Mark where platelets are.
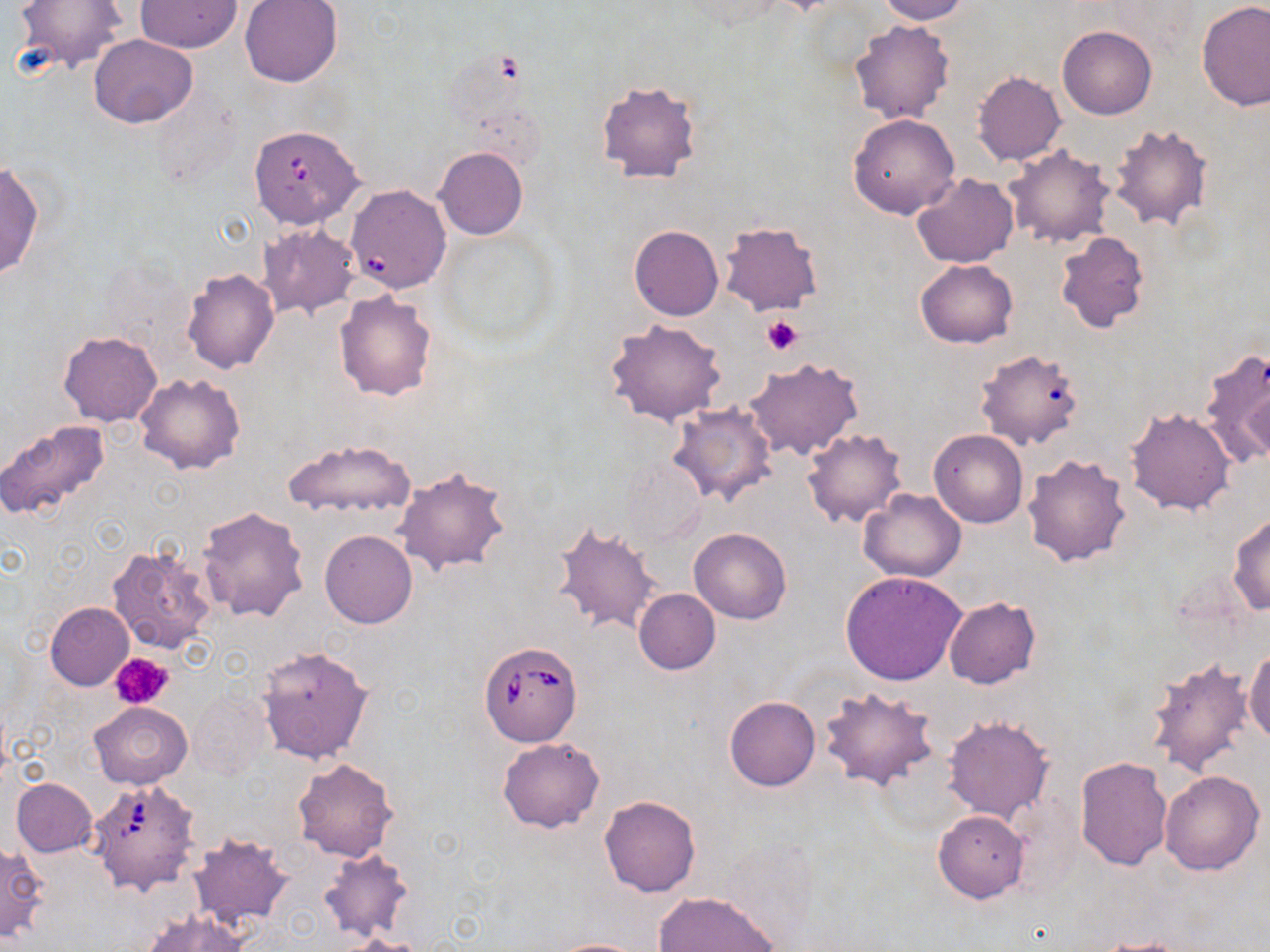

Approximate bounding boxes as (x1,y1)-(x2,y2) corner pairs in pixels.
Platelets: (762,315)-(802,355), (111,652)-(175,710).

Summary:
  - Uninfected red blood cell locations: (14,0)-(128,74), (240,0)-(343,87), (877,0)-(969,24), (136,1)-(241,52), (672,1)-(789,32), (1196,1)-(1270,113), (849,19)-(954,125), (1058,25)-(1156,120), (90,34)-(198,128), (973,71)-(1065,165), (595,79)-(703,185), (849,113)-(959,219), (1107,122)-(1213,231), (1003,145)-(1115,249), (435,147)-(527,241), (0,162)-(43,282), (911,173)-(1019,268), (717,221)-(824,316), (258,222)-(361,319), (629,225)-(723,321), (1054,231)-(1150,333), (915,259)-(1018,348), (181,268)-(280,374), (334,290)-(438,401), (604,319)-(729,428), (58,332)-(162,426), (1200,344)-(1270,468), (974,348)-(1084,450), (742,357)-(863,460), (135,373)-(246,475), (668,404)-(777,505), (1125,406)-(1237,516), (0,421)-(111,524), (802,429)-(908,528), (930,430)-(1029,528), (285,439)-(416,519), (1020,453)-(1132,568), (620,459)-(707,550), (393,466)-(510,575), (859,488)-(966,581), (196,505)-(309,624), (1228,513)-(1270,616), (552,521)-(663,638), (689,528)-(791,624), (320,530)-(417,628), (106,544)-(216,653), (841,570)-(967,686), (634,589)-(720,674), (943,595)-(1041,690), (45,602)-(134,690), (255,646)-(373,764), (1245,647)-(1270,748), (1145,655)-(1256,780), (819,686)-(938,790), (189,688)-(273,780), (724,695)-(820,791), (89,702)-(191,789), (942,714)-(1053,824), (498,737)-(604,833), (1074,757)-(1171,871), (292,758)-(398,862), (1160,769)-(1264,875), (10,778)-(97,857), (598,795)-(701,897), (933,809)-(1030,903), (187,833)-(293,927), (0,843)-(47,941), (320,847)-(414,941), (652,891)-(781,952), (142,911)-(250,952), (345,934)-(428,952), (1084,935)-(1195,951), (544,937)-(651,951)
  - Babesia divergens-infected red blood cell locations: (246,124)-(370,237), (352,187)-(457,300), (479,642)-(583,746), (89,779)-(200,895)
  - Slide-level diagnosis: Babesia divergens
  - Modality: optical microscopy
  - Preparation: thin blood film
  - Field of view: single
  - Magnification: 1000x
  - Image size: 1270×952 pixels
  - Stain: May-Grünwald-Giemsa